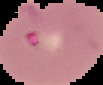

Segmented cell region on a black background. Result: Plasmodium parasites identified. From a thin blood smear. Image is 103×85 pixels.